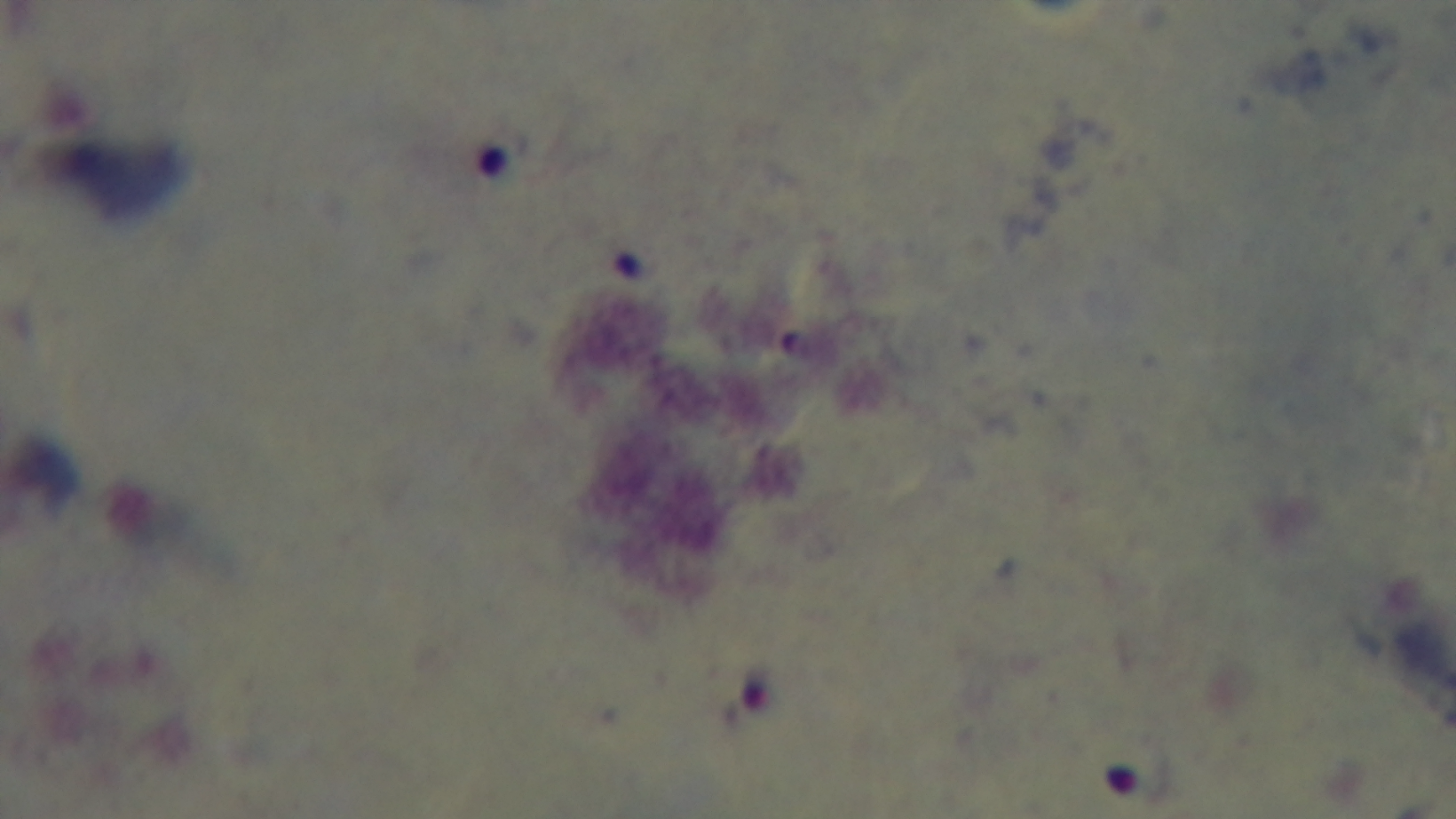

Malaria status: positive. Preparation: thick. Giemsa-stained. One field from the slide. Oil-immersion objective, 100x. Captured with a mounted 4K digital camera. Photomicrograph.